Assess this cell for malaria.
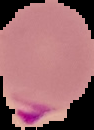

Parasitized.

image type = segmented cell region on a black background
preparation = thin blood smear
image size = 94×130 pixels